Report the malaria status of this cell.
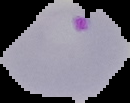

Parasitized.

Summary:
  - Image type: segmented cell region on a black background
  - Preparation: thin blood smear
  - Image size: 130×103 pixels